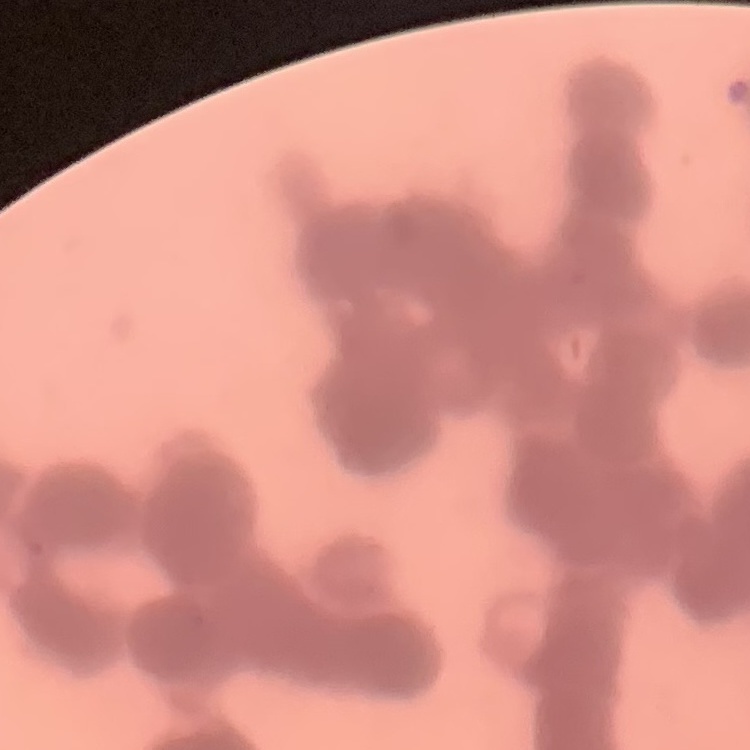

Summary:
  - Erythrocyte morphology: rouleaux formation
  - Preparation: thin peripheral smear
  - Image type: square crop of a larger photomicrograph
  - Stain: Field's or Giemsa